Assess for Plasmodium parasites.
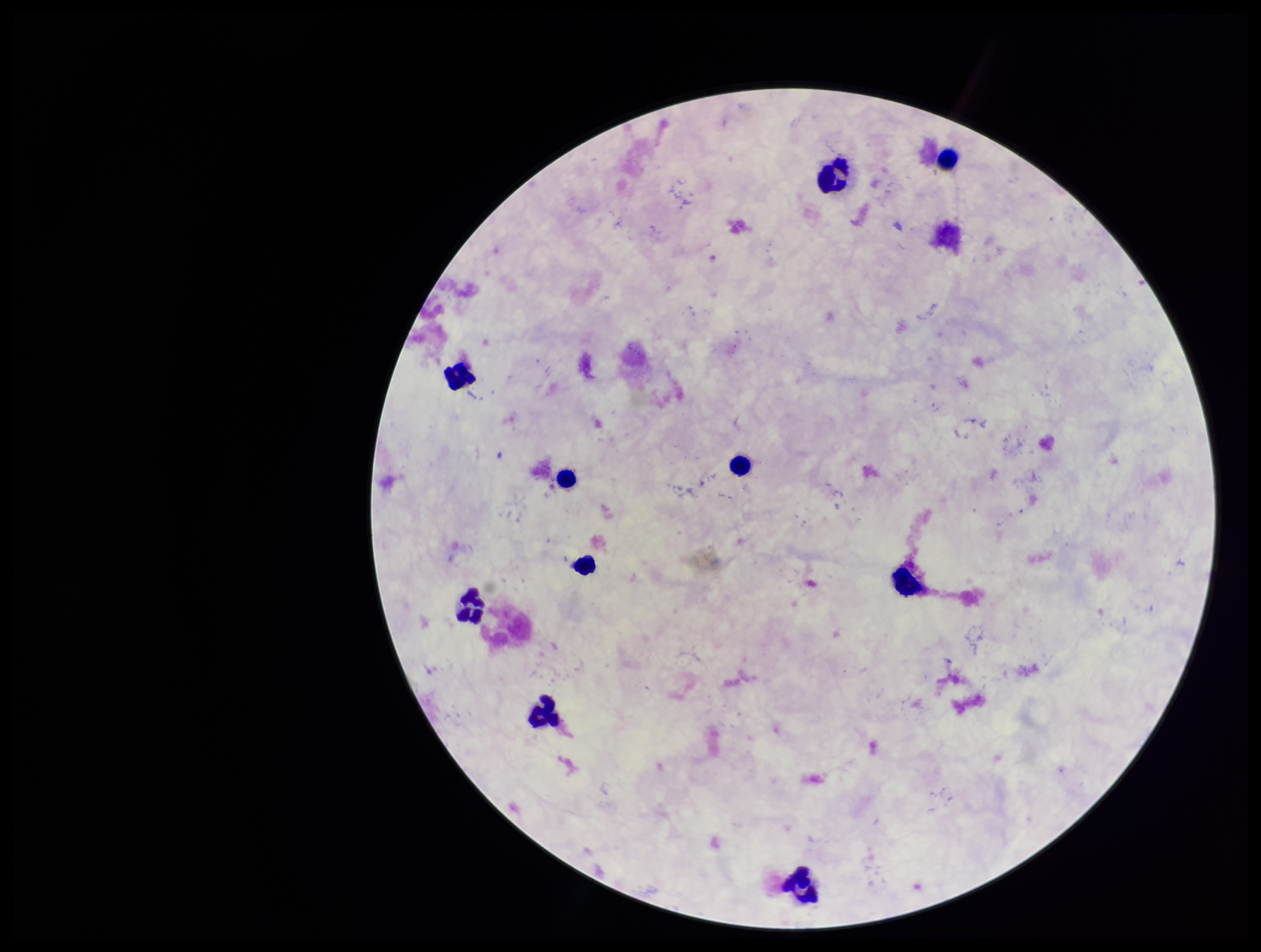

None detected.

Parasite count: 0. Stained with Giemsa. Leukocyte count: 10. Preparation: thick. One field from this slide. Photographed through the microscope eyepiece with a smartphone camera. Patient malaria status: negative. Image is 1261×952 pixels.